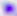 Captured at 400x magnification. Toxoplasma gondii is shown. Photomicrograph.